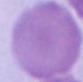

Micrograph. An erythrocyte is seen. 1000x magnification.